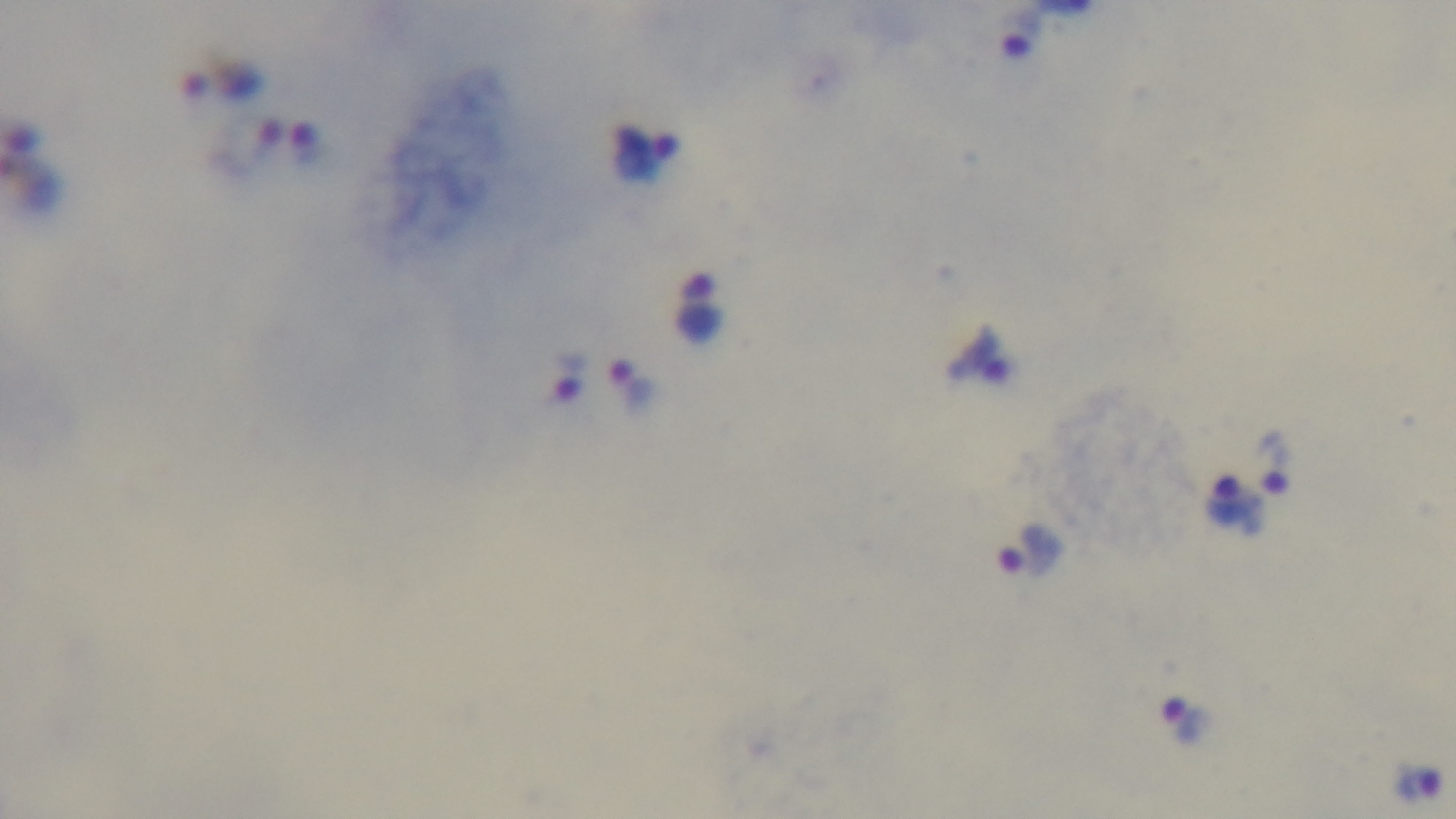
stain = Giemsa
preparation = thick blood film
modality = light microscopy
objective = 100x oil immersion
capture = mounted 4K digital camera
field of view = single
malaria status = positive